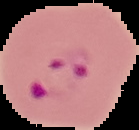 Image is 139×130 pixels. From a thin blood film. Malaria status: parasitized. Segmented cell region on a black background.